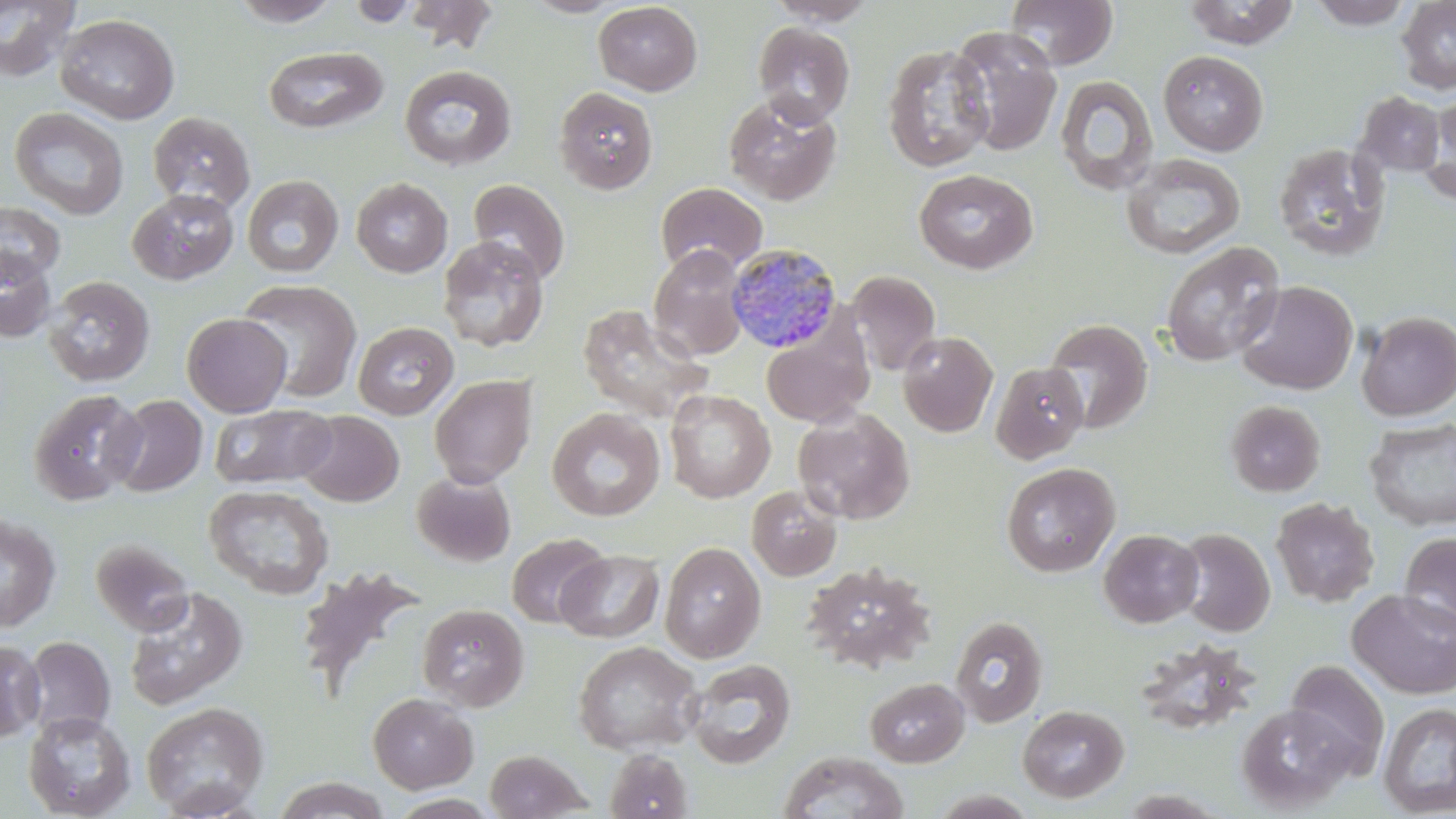
Summary:
  - Coordinate format: approximate bounding boxes as named x1/y1/x2/y2 corners in pixels
  - Uninfected red blood cell locations: (x1=0, y1=0, x2=82, y2=83), (x1=229, y1=0, x2=342, y2=27), (x1=346, y1=0, x2=422, y2=27), (x1=401, y1=0, x2=499, y2=54), (x1=522, y1=0, x2=627, y2=18), (x1=764, y1=0, x2=879, y2=26), (x1=1005, y1=0, x2=1119, y2=70), (x1=1182, y1=0, x2=1300, y2=48), (x1=1307, y1=0, x2=1415, y2=29), (x1=1396, y1=0, x2=1456, y2=95), (x1=594, y1=2, x2=702, y2=96), (x1=54, y1=13, x2=180, y2=125), (x1=752, y1=21, x2=855, y2=127), (x1=948, y1=26, x2=1063, y2=157), (x1=882, y1=43, x2=994, y2=172), (x1=263, y1=46, x2=388, y2=134), (x1=1158, y1=50, x2=1269, y2=156), (x1=399, y1=65, x2=517, y2=170), (x1=1054, y1=74, x2=1159, y2=196), (x1=553, y1=86, x2=659, y2=195), (x1=1356, y1=91, x2=1445, y2=177), (x1=1424, y1=92, x2=1456, y2=204), (x1=723, y1=94, x2=842, y2=207), (x1=9, y1=107, x2=129, y2=220), (x1=148, y1=111, x2=255, y2=213), (x1=1272, y1=142, x2=1391, y2=261), (x1=1120, y1=153, x2=1246, y2=260), (x1=914, y1=169, x2=1038, y2=274), (x1=241, y1=175, x2=343, y2=277), (x1=351, y1=177, x2=453, y2=278), (x1=468, y1=179, x2=570, y2=285), (x1=655, y1=181, x2=768, y2=276), (x1=127, y1=189, x2=239, y2=285), (x1=0, y1=201, x2=65, y2=285), (x1=437, y1=236, x2=549, y2=353), (x1=1161, y1=242, x2=1284, y2=366), (x1=649, y1=244, x2=750, y2=361), (x1=0, y1=248, x2=58, y2=343), (x1=846, y1=270, x2=941, y2=377), (x1=42, y1=276, x2=156, y2=388), (x1=235, y1=278, x2=362, y2=403), (x1=1236, y1=280, x2=1358, y2=395), (x1=576, y1=304, x2=712, y2=423), (x1=1356, y1=310, x2=1456, y2=421), (x1=182, y1=313, x2=292, y2=417), (x1=1042, y1=318, x2=1152, y2=434), (x1=352, y1=321, x2=458, y2=420), (x1=760, y1=324, x2=873, y2=428), (x1=898, y1=331, x2=998, y2=437), (x1=990, y1=361, x2=1090, y2=464), (x1=429, y1=374, x2=537, y2=488), (x1=28, y1=389, x2=145, y2=506), (x1=664, y1=389, x2=775, y2=503), (x1=107, y1=394, x2=208, y2=497), (x1=1225, y1=400, x2=1325, y2=497), (x1=210, y1=404, x2=337, y2=489), (x1=547, y1=408, x2=665, y2=521), (x1=792, y1=408, x2=915, y2=524), (x1=296, y1=410, x2=404, y2=507), (x1=1364, y1=417, x2=1456, y2=531), (x1=1001, y1=462, x2=1120, y2=577), (x1=411, y1=472, x2=516, y2=567), (x1=204, y1=484, x2=334, y2=600), (x1=746, y1=485, x2=842, y2=581), (x1=1271, y1=497, x2=1379, y2=607), (x1=0, y1=514, x2=61, y2=632), (x1=1176, y1=527, x2=1275, y2=637), (x1=1098, y1=528, x2=1204, y2=628), (x1=1399, y1=532, x2=1456, y2=634), (x1=506, y1=534, x2=609, y2=628), (x1=90, y1=539, x2=194, y2=635), (x1=660, y1=541, x2=766, y2=663), (x1=555, y1=550, x2=664, y2=642), (x1=802, y1=562, x2=938, y2=673), (x1=292, y1=565, x2=428, y2=702), (x1=123, y1=587, x2=248, y2=711), (x1=1347, y1=589, x2=1456, y2=700), (x1=416, y1=603, x2=529, y2=711), (x1=950, y1=615, x2=1048, y2=727), (x1=22, y1=635, x2=114, y2=740), (x1=0, y1=639, x2=45, y2=741), (x1=573, y1=640, x2=702, y2=755), (x1=684, y1=659, x2=796, y2=769), (x1=1285, y1=660, x2=1390, y2=774), (x1=864, y1=676, x2=968, y2=768), (x1=367, y1=692, x2=478, y2=793), (x1=141, y1=701, x2=270, y2=817), (x1=1378, y1=702, x2=1456, y2=816), (x1=1017, y1=704, x2=1129, y2=803), (x1=1235, y1=704, x2=1357, y2=812), (x1=23, y1=711, x2=136, y2=818), (x1=483, y1=749, x2=591, y2=818), (x1=604, y1=749, x2=694, y2=819), (x1=776, y1=750, x2=910, y2=819), (x1=272, y1=776, x2=390, y2=818)
  - Plasmodium malariae-infected red blood cell locations: (x1=725, y1=241, x2=844, y2=353)
  - Slide-level diagnosis: Plasmodium malariae
  - Preparation: thin blood film
  - Modality: light microscopy
  - Field of view: single
  - Magnification: 1000x
  - Stain: May-Grünwald-Giemsa
  - Image size: 1456×819 pixels